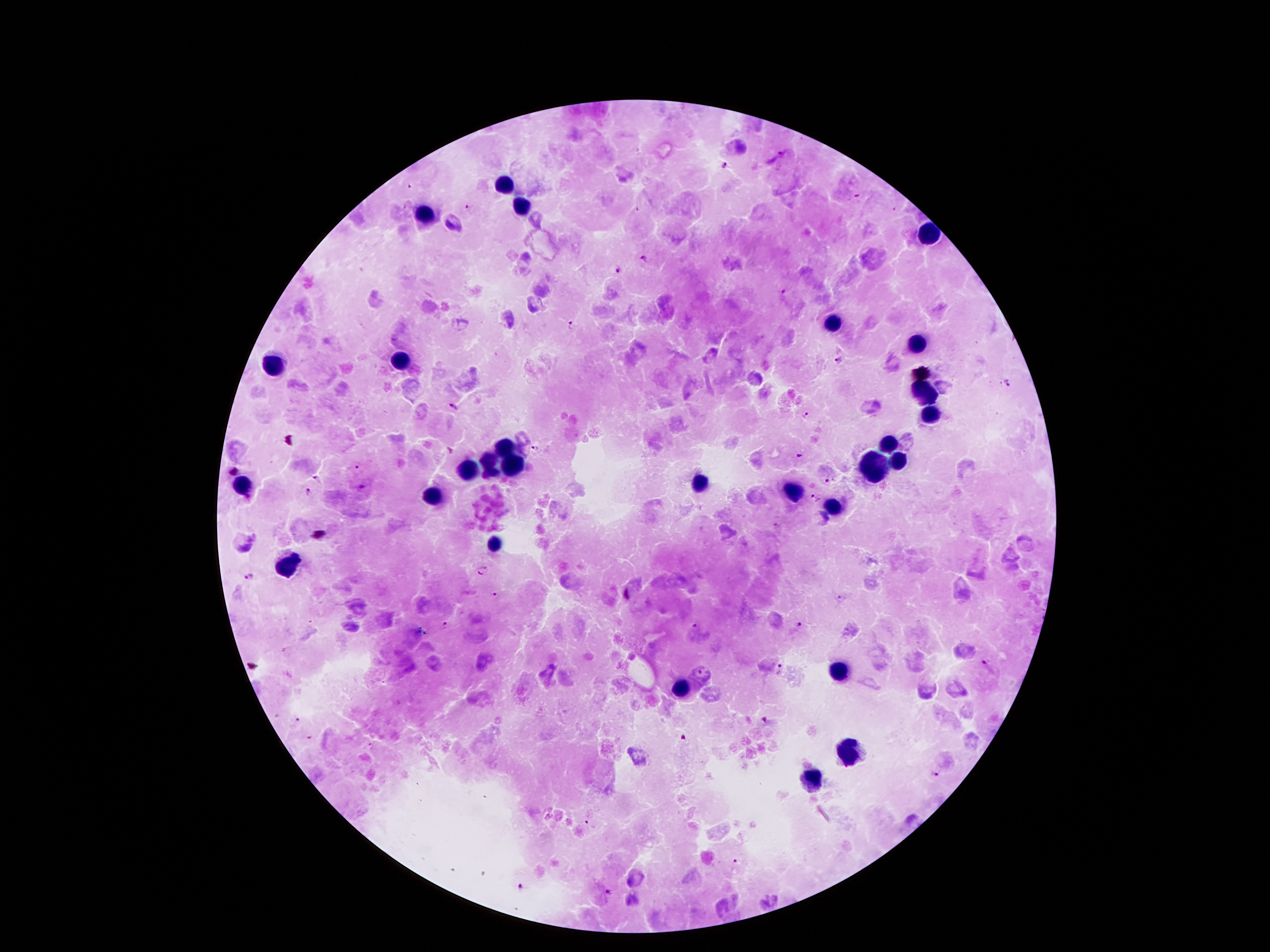

Approximate centers as [x, y] in pixels.
Summary:
  - Malaria parasite locations: [727, 164], [410, 184], [469, 206], [644, 257], [619, 269], [785, 290], [571, 323], [839, 359], [1006, 382], [452, 406], [806, 415], [536, 448], [797, 455], [356, 464], [233, 470], [317, 478], [827, 479], [361, 486], [308, 493], [815, 497], [485, 571], [248, 578], [494, 592], [841, 599], [445, 625], [694, 625], [799, 626], [985, 665], [779, 668], [766, 719], [298, 721], [310, 737], [937, 776], [587, 821], [736, 860], [520, 887], [608, 892]
  - Leukocyte locations: [504, 184], [521, 206], [423, 211], [932, 235], [828, 324], [919, 342], [400, 359], [272, 361], [929, 391], [932, 413], [502, 441], [887, 443], [487, 460], [897, 460], [514, 465], [872, 465], [467, 470], [699, 483], [242, 485], [793, 490], [435, 495], [833, 505], [494, 544], [287, 566], [838, 670], [680, 688], [850, 749], [808, 781]
  - Image size: 1270×952 pixels
  - Stain: Giemsa
  - Capture: smartphone camera through the microscope eyepiece
  - Patient malaria status: positive for Plasmodium falciparum
  - Preparation: thick blood film
  - Field of view: one from this slide
  - Magnification: 100x